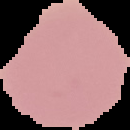
Summary:
  - Image type: cell region segmented out of the field of view; surrounding area masked to black
  - Malaria status: uninfected
  - Image size: 130×130 pixels
  - Preparation: thin blood film